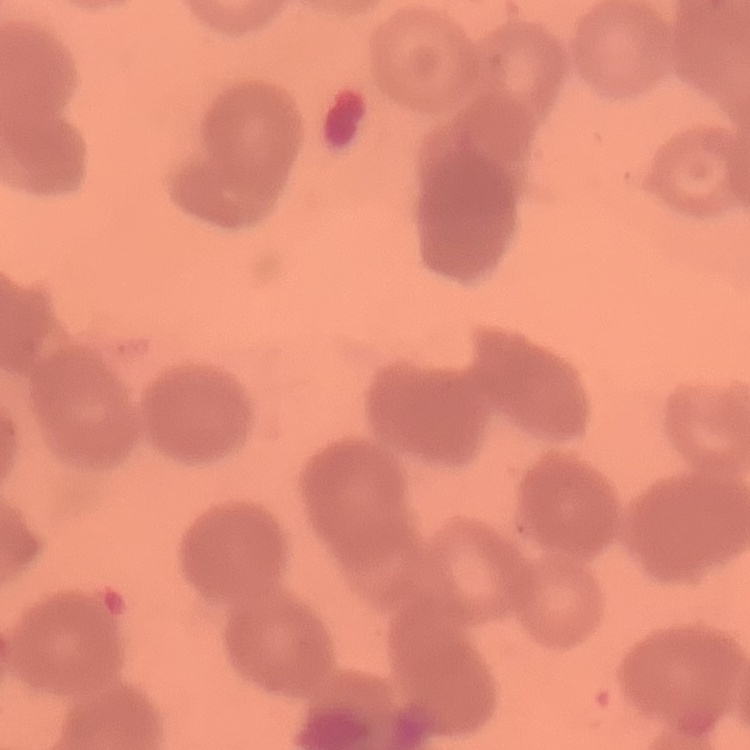

Summary:
  - Erythrocyte morphology: rouleaux formation
  - Preparation: thin blood film
  - Stain: Field's or Giemsa
  - Image type: square crop of a larger photomicrograph